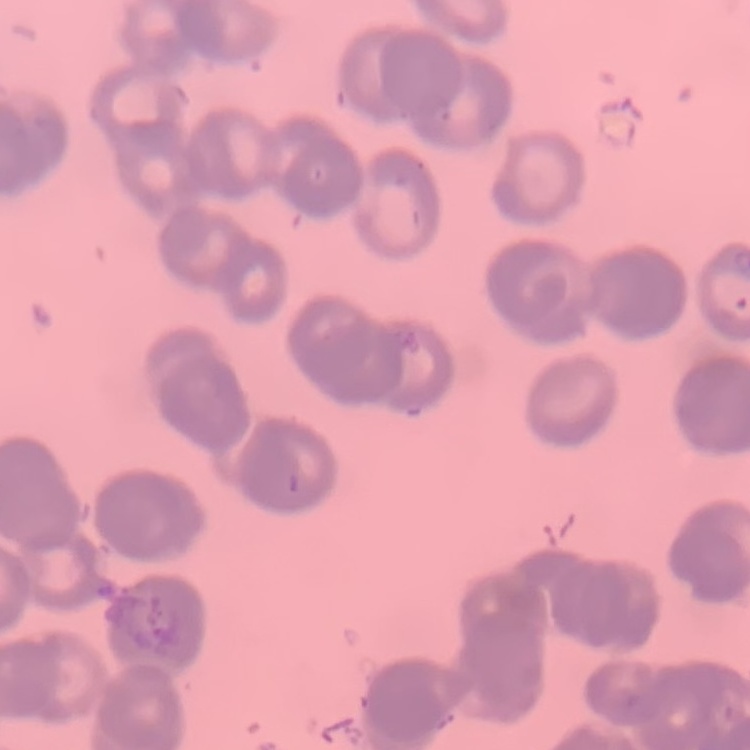
red_blood_cell_morphology: rouleaux formation
stain: Field's or Giemsa
image_type: square crop of a larger photomicrograph
preparation: thin blood smear